Comment on the morphology of the erythrocytes.
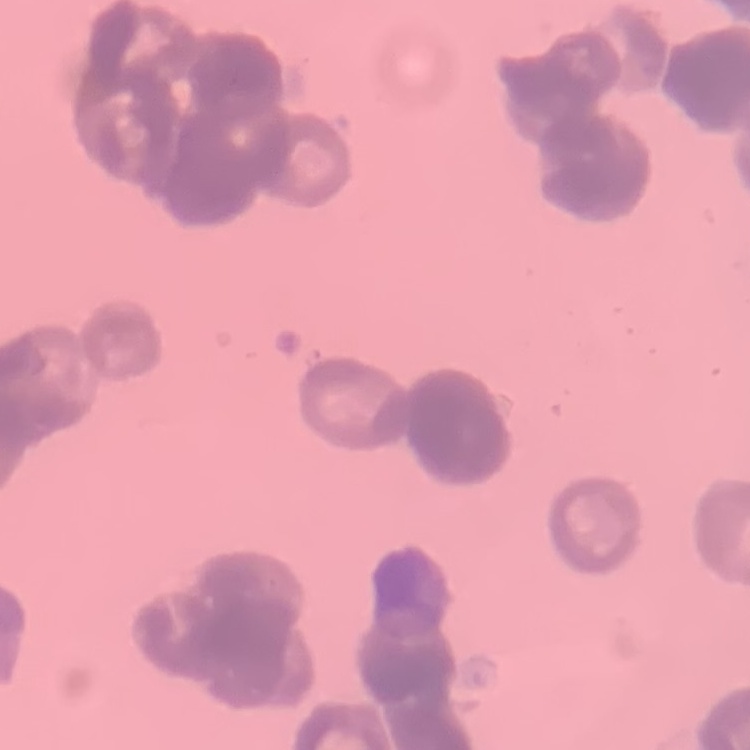
Rouleaux formation.

Summary:
  - Stain: Field's or Giemsa
  - Preparation: thin peripheral smear
  - Image type: one tile cut from a larger photomicrograph